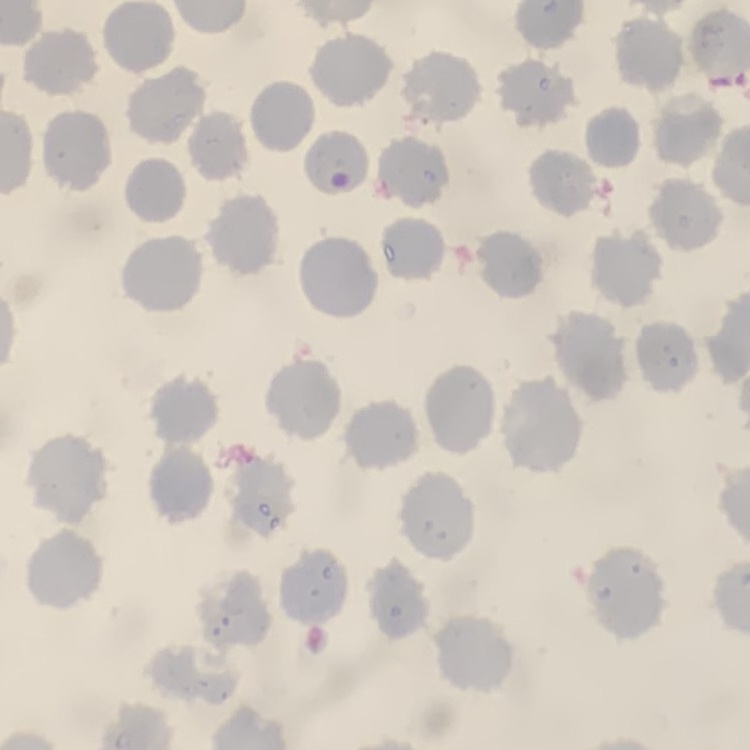 The red blood cells exhibit no rouleaux formation. Square crop of a larger photomicrograph. Field's or Giemsa stain. Thin peripheral smear.